Classify this cell by malaria status.
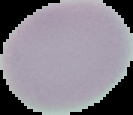

Uninfected.

image size = 133×115 pixels
image type = cell region segmented out of the field of view; surrounding area masked to black
preparation = thin blood smear